Assess this cell for malaria.
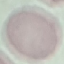

It is uninfected.

{
  "capture": "smartphone through the microscope eyepiece",
  "stain": "Giemsa",
  "preparation": "thin blood smear",
  "image_type": "automatically extracted cell patch, resized to 64 × 64 pixels"
}